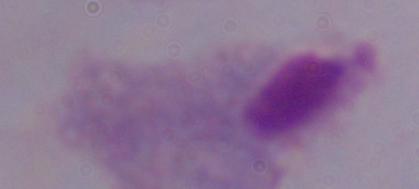
Summary:
  - Identification: trichomonad
  - Magnification: 1000x
  - Modality: micrograph